Locate and identify every blood parasite.
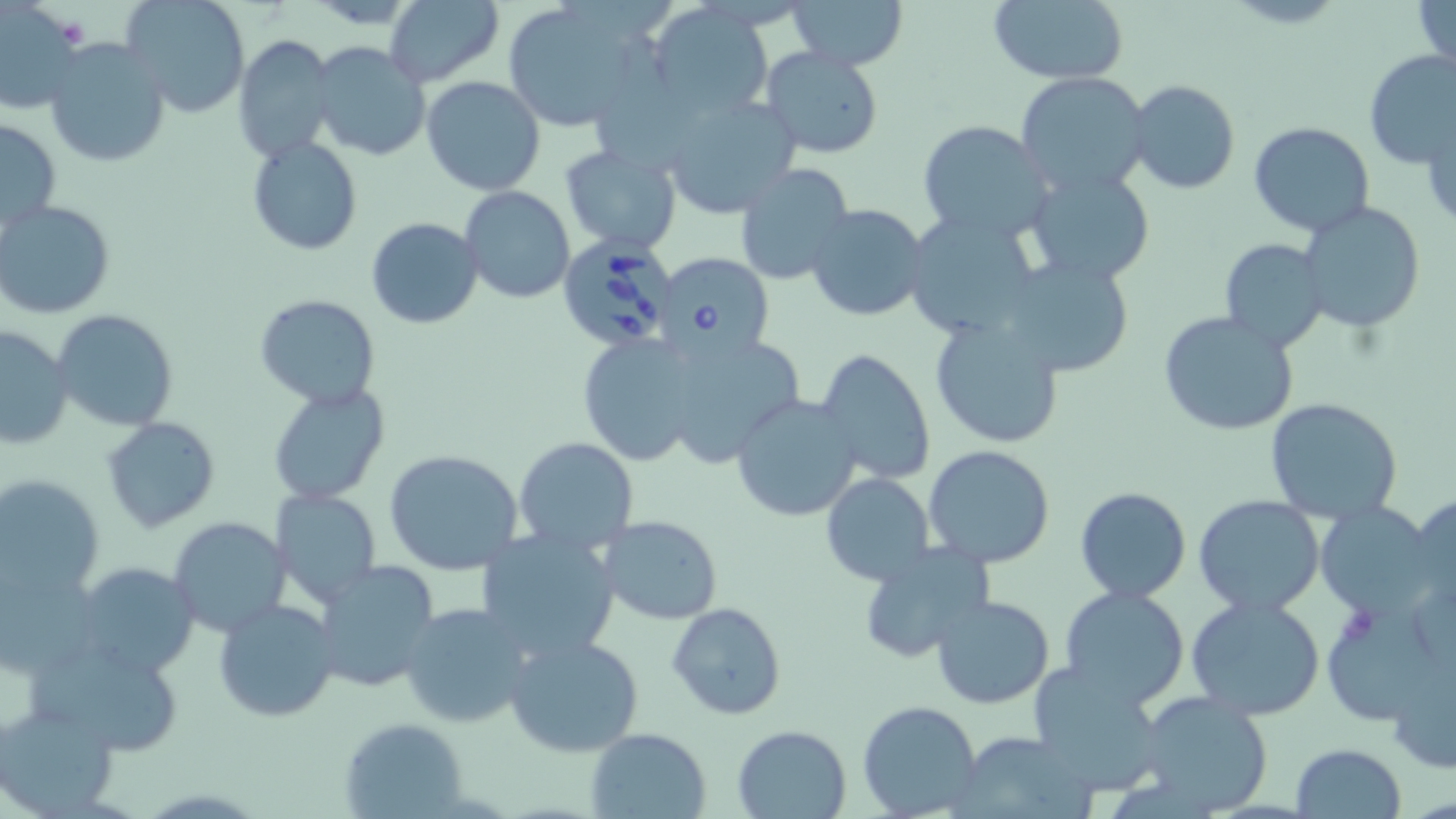

Approximate bounding boxes as [x1, y1, x2, y2] in pixels.
Babesia divergens-infected red blood cells: [555, 232, 679, 354], [655, 252, 774, 361].
No Plasmodium falciparum, Plasmodium ovale, Plasmodium malariae, Plasmodium vivax, or Trypanosoma brucei observed.

Uninfected red blood cell locations: [122, 0, 250, 118], [500, 0, 650, 133], [787, 0, 908, 71], [986, 0, 1129, 86], [1413, 0, 1455, 75], [306, 1, 425, 28], [385, 1, 504, 87], [648, 2, 774, 120], [2, 9, 86, 117], [231, 34, 337, 163], [42, 38, 172, 168], [309, 42, 432, 161], [759, 47, 885, 160], [1363, 48, 1456, 167], [1013, 70, 1151, 197], [421, 75, 547, 195], [1125, 79, 1241, 196], [657, 92, 801, 216], [921, 95, 1155, 227], [1423, 110, 1456, 227], [1, 116, 62, 238], [917, 119, 1054, 242], [1269, 121, 1400, 331], [695, 122, 832, 264], [1248, 122, 1376, 237], [248, 138, 362, 255], [559, 145, 682, 255], [733, 162, 855, 288], [1022, 164, 1157, 284], [461, 186, 575, 303], [0, 200, 116, 319], [1299, 201, 1426, 334], [803, 202, 931, 323], [902, 209, 1043, 342], [365, 216, 483, 329], [1219, 239, 1328, 353], [997, 252, 1135, 379], [253, 293, 380, 408], [52, 309, 180, 431], [1158, 309, 1299, 436], [929, 317, 1066, 448], [1, 324, 74, 450], [647, 327, 807, 468], [576, 333, 705, 466], [813, 348, 937, 485], [267, 383, 391, 507], [730, 395, 862, 523], [1264, 397, 1403, 525], [101, 416, 220, 533], [512, 436, 640, 554], [923, 445, 1057, 568], [385, 450, 526, 576], [821, 473, 935, 589], [0, 474, 105, 601], [1075, 486, 1192, 602], [271, 489, 382, 609], [1406, 492, 1456, 611], [1193, 494, 1326, 616], [1315, 502, 1443, 620], [597, 514, 724, 626], [169, 516, 291, 638], [475, 528, 621, 663], [857, 542, 997, 664], [312, 560, 441, 693], [73, 562, 200, 677], [0, 563, 101, 676], [1057, 586, 1190, 710], [1320, 592, 1451, 728], [930, 594, 1057, 710], [1186, 596, 1327, 720], [212, 599, 340, 722], [665, 601, 787, 721], [399, 602, 533, 729], [503, 633, 644, 758], [23, 634, 185, 752], [1389, 649, 1456, 778], [1029, 660, 1169, 793], [1134, 690, 1275, 815], [858, 701, 983, 819], [0, 702, 120, 816], [338, 717, 471, 818], [731, 724, 852, 818], [585, 727, 711, 819], [955, 731, 1095, 817], [1289, 743, 1407, 819]. Slide-level diagnosis: Babesia divergens. Optical microscopy. 1000x magnification. Thin blood smear. Single field of view. May-Grünwald-Giemsa stain. Image is 1456×819 pixels.